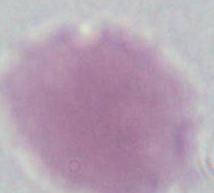

magnification = 1000x
modality = micrograph
identification = red blood cell